Name the blood parasite species.
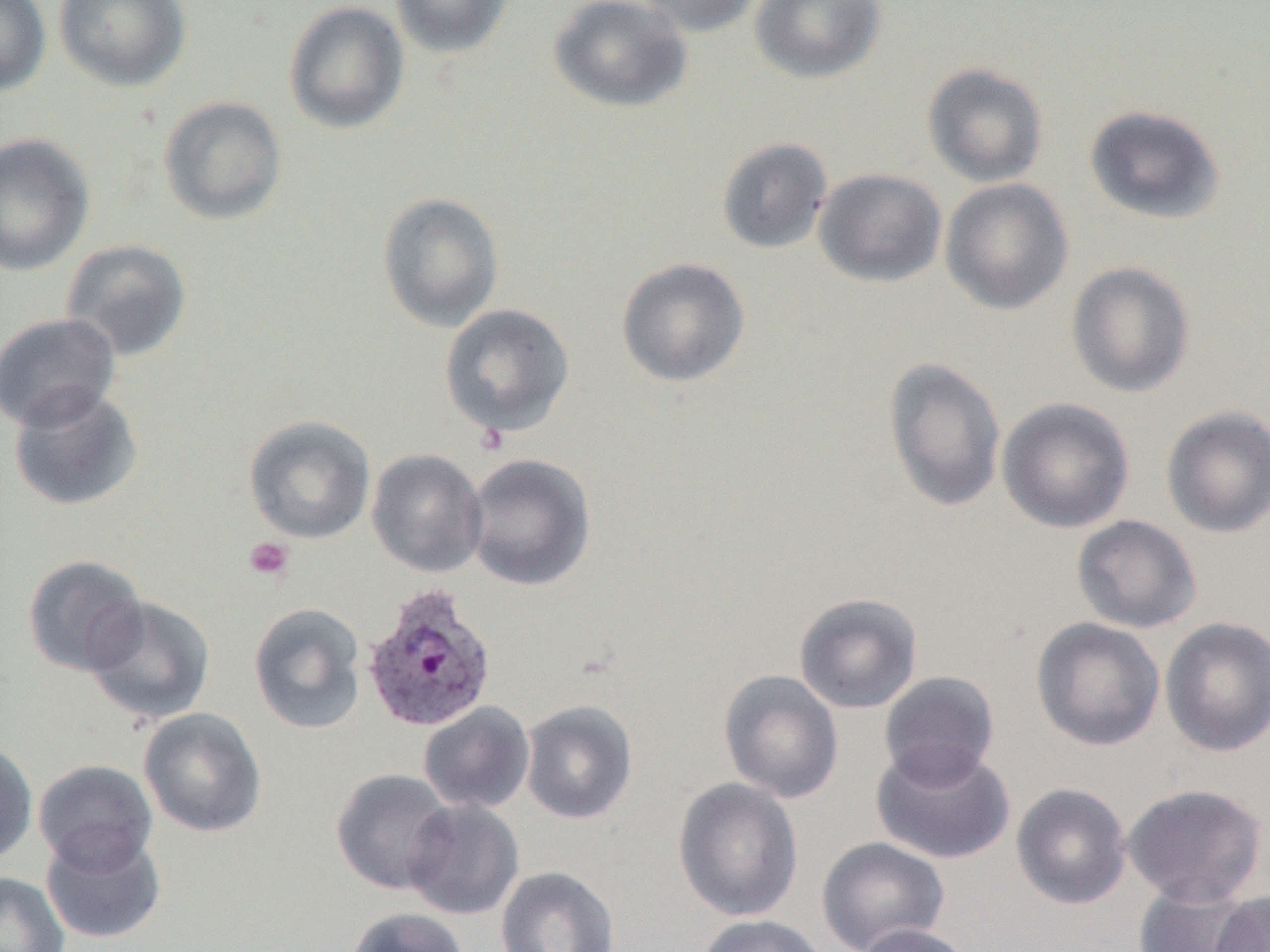
Plasmodium ovale.

platelet_locations: 'approximate bounding boxes as (x1, y1, x2, y2) in pixels: (244, 537, 294, 582)'
magnification: 1000x
field_of_view: single
plasmodium_ovale_infected_red_blood_cell_locations: 'approximate bounding boxes as (x1, y1, x2, y2) in pixels: (361, 584, 498, 733)'
image_size: 1270×952 pixels
modality: optical microscopy
preparation: thin blood smear
uninfected_red_blood_cell_locations: 'approximate bounding boxes as (x1, y1, x2, y2) in pixels: (0, 0, 50, 96), (53, 0, 192, 92), (389, 0, 514, 59), (549, 0, 693, 113), (633, 0, 765, 37), (750, 0, 886, 84), (283, 1, 410, 134), (921, 63, 1049, 187), (158, 96, 287, 225), (1084, 104, 1226, 225), (0, 133, 96, 277), (716, 137, 833, 255), (814, 168, 947, 287), (940, 178, 1074, 315), (377, 191, 505, 332), (60, 239, 193, 362), (616, 257, 751, 387), (1066, 261, 1195, 398), (439, 303, 575, 438), (0, 312, 121, 432), (882, 355, 1007, 513), (7, 385, 144, 512), (997, 397, 1135, 534), (1161, 406, 1270, 539), (244, 414, 376, 544), (367, 448, 488, 577), (465, 452, 596, 592), (1072, 515, 1202, 633), (21, 554, 148, 678), (794, 592, 923, 714), (84, 596, 216, 726), (248, 602, 367, 735), (1030, 616, 1166, 751), (1159, 616, 1270, 757), (718, 669, 844, 804), (879, 671, 1000, 786), (520, 699, 638, 824), (418, 702, 535, 814), (138, 708, 267, 838), (0, 739, 38, 865), (872, 743, 1015, 865), (33, 758, 158, 875), (330, 768, 457, 895), (673, 777, 804, 923), (1010, 782, 1132, 910), (1122, 783, 1268, 907), (403, 799, 525, 920), (41, 829, 167, 944), (816, 836, 950, 952), (495, 866, 620, 952), (0, 872, 70, 952), (1133, 879, 1262, 952), (1210, 891, 1270, 952), (345, 907, 471, 952), (693, 914, 832, 952), (855, 922, 975, 952)'